Assess this cell for malaria.
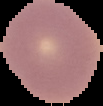

It is uninfected.

Summary:
  - Image size: 103×106 pixels
  - Image type: segmented cell region with the area outside set to black
  - Preparation: thin blood smear